Locate platelets.
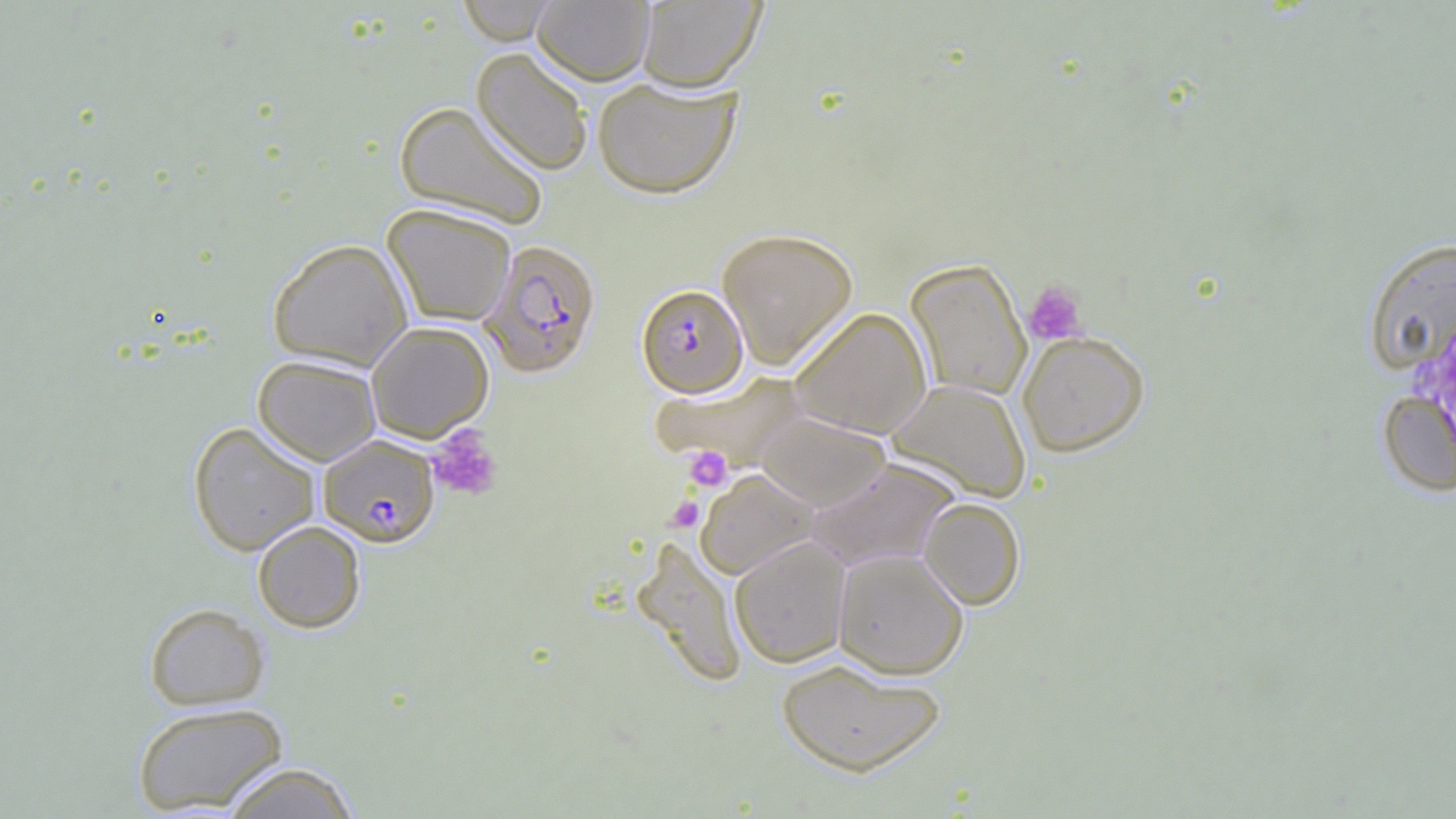

Approximate bounding boxes as (x1,y1)-(x2,y2) corner pairs in pixels.
Platelets: (1022,281)-(1087,346), (427,425)-(503,502), (682,445)-(733,492), (666,495)-(704,532).

Summary:
  - Uninfected red blood cell locations: (456,0)-(561,45), (532,0)-(655,85), (636,0)-(765,91), (471,47)-(593,177), (591,76)-(742,199), (394,101)-(549,230), (382,203)-(517,327), (716,227)-(858,370), (1363,236)-(1455,375), (267,238)-(413,371), (906,259)-(1032,402), (789,307)-(932,438), (365,321)-(494,442), (1017,329)-(1150,457), (253,354)-(381,466), (655,371)-(807,469), (887,378)-(1032,503), (1377,389)-(1456,499), (754,411)-(893,511), (188,421)-(321,556), (806,458)-(961,573), (694,468)-(820,579), (918,497)-(1025,610), (252,520)-(366,633), (631,536)-(749,688), (729,537)-(850,668), (833,548)-(969,679), (144,602)-(270,710), (776,659)-(947,777), (132,701)-(288,814), (219,761)-(361,819)
  - Plasmodium falciparum-infected red blood cell locations: (479,239)-(602,378), (636,283)-(749,398), (318,435)-(440,546)
  - Slide-level diagnosis: Plasmodium falciparum
  - Field of view: one of a larger specimen
  - Magnification: 1000x
  - Preparation: thin blood film
  - Modality: light microscopy
  - Image size: 1456×819 pixels